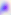

modality = micrograph
magnification = 400x
identification = Toxoplasma gondii